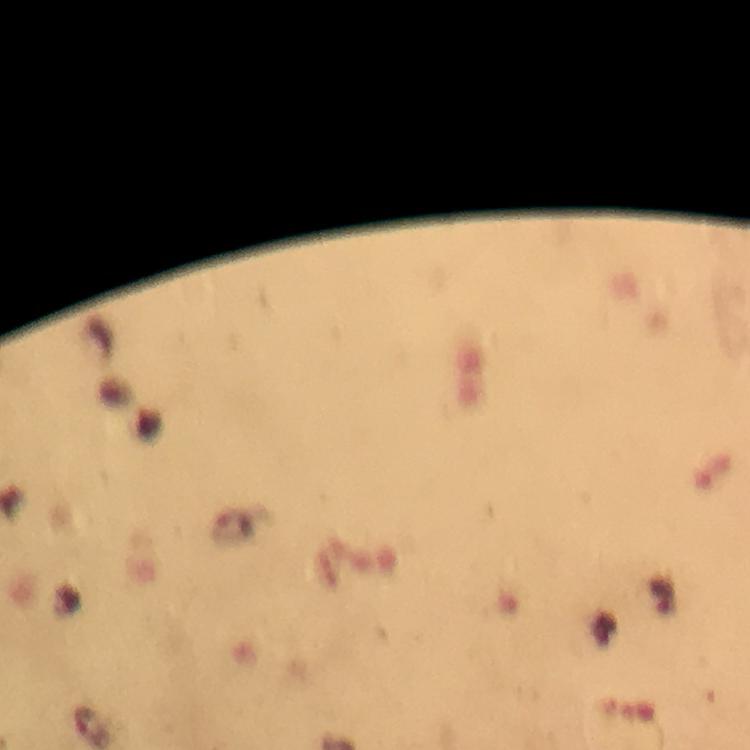

Approximate centers as (x, y) in pixels. Malaria parasite locations: (93, 726). Image is 750×750 pixels. Giemsa stain. At 100x magnification. Cropped region of a single field of view. From a diagnostic examination for malaria. Immersion oil applied. Thick blood film. Photographed through the microscope with a smartphone camera.